Report the malaria status of this cell.
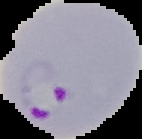
It is parasitized.

From a thin blood smear. Image is 142×139 pixels. Cell region segmented out of the field of view; the surrounding area is masked to black.